Evaluate for Plasmodium parasites.
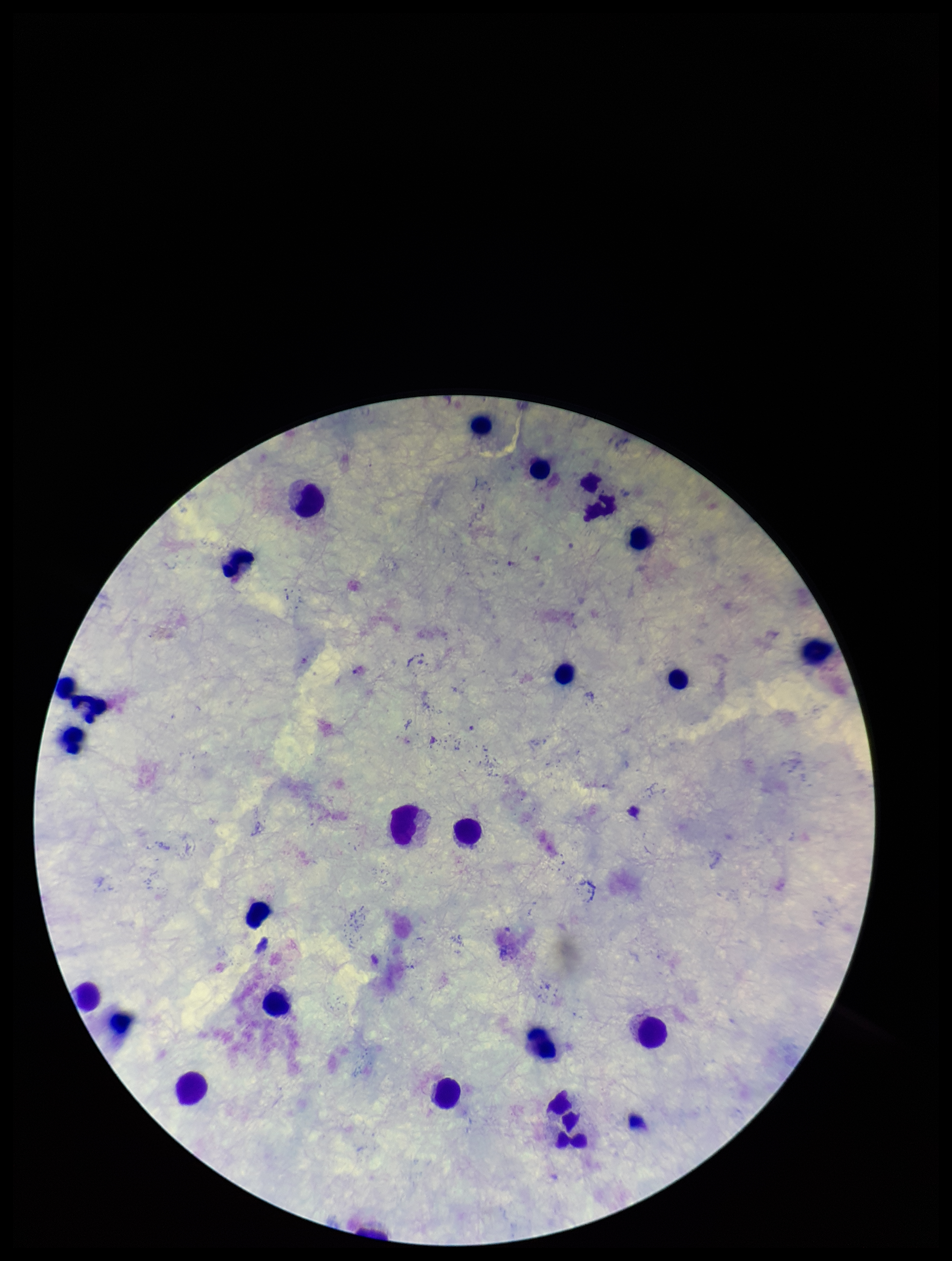
None identified.

Summary:
  - Leukocyte count: 24
  - Image size: 952×1261 pixels
  - Patient malaria status: negative
  - Field of view: one from this slide
  - Capture: smartphone photograph through the microscope eyepiece
  - Preparation: thick
  - Stain: Giemsa
  - Parasite count: 0